Assess the morphology of the erythrocytes.
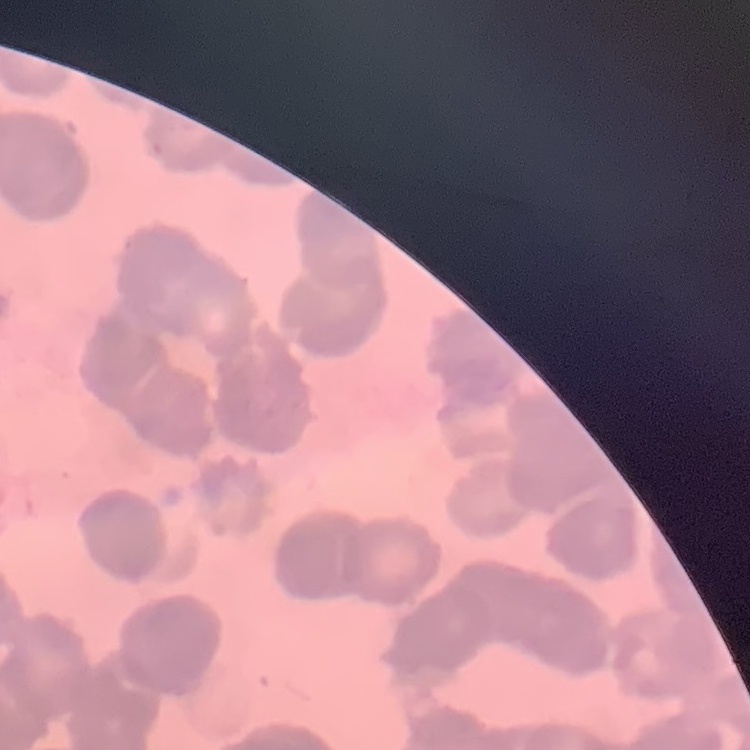

Rouleaux formation.

Thin peripheral smear. Stained with either Field's or Giemsa. Square crop of a larger photomicrograph.